Name the blood parasite species.
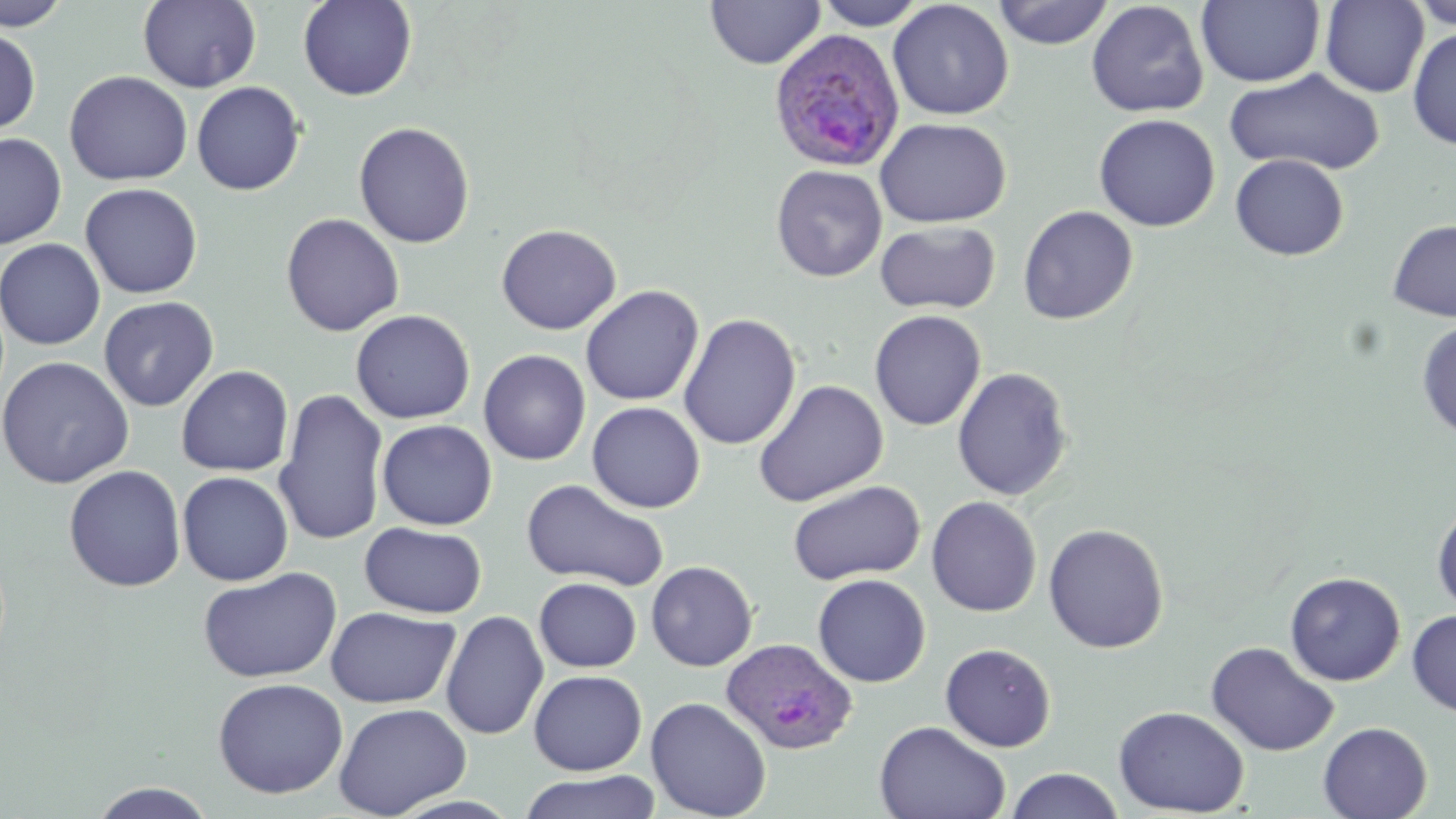

Plasmodium ovale.

uninfected red blood cell locations = approximate bounding boxes as (x1, y1, x2, y2) in pixels: (0, 0, 73, 31), (138, 0, 262, 93), (298, 0, 417, 101), (705, 0, 825, 69), (813, 0, 929, 30), (992, 0, 1114, 49), (1408, 0, 1455, 31), (888, 1, 1013, 120), (1086, 1, 1209, 118), (1196, 1, 1325, 87), (1320, 1, 1429, 97), (1407, 25, 1456, 150), (0, 26, 41, 137), (1224, 68, 1385, 177), (64, 71, 192, 186), (191, 81, 306, 196), (1093, 113, 1220, 232), (875, 117, 1011, 228), (353, 122, 475, 249), (0, 132, 67, 249), (1230, 154, 1348, 260), (771, 165, 887, 283), (80, 182, 203, 299), (1017, 205, 1138, 325), (280, 213, 404, 337), (1387, 218, 1456, 322), (875, 220, 1000, 315), (496, 224, 621, 335), (0, 238, 105, 350), (580, 285, 704, 406), (98, 296, 219, 412), (350, 309, 475, 424), (869, 309, 986, 431), (678, 313, 801, 450), (1416, 319, 1456, 439), (478, 349, 591, 466), (0, 356, 135, 489), (176, 365, 294, 477), (952, 367, 1073, 501), (753, 379, 888, 507), (273, 389, 390, 547), (586, 402, 705, 513), (376, 419, 497, 531), (63, 465, 186, 592), (177, 471, 294, 586), (521, 479, 670, 592), (787, 480, 925, 585), (926, 496, 1042, 617), (1432, 500, 1456, 615), (360, 522, 487, 618), (1043, 523, 1169, 653), (646, 561, 758, 671), (197, 567, 343, 684), (1285, 571, 1406, 685), (812, 574, 931, 687), (534, 577, 642, 672), (325, 606, 460, 708), (440, 610, 549, 741), (1407, 610, 1456, 718), (1205, 641, 1339, 756), (940, 643, 1056, 752), (528, 669, 647, 776), (212, 677, 348, 799), (645, 696, 771, 819), (333, 703, 472, 818), (1113, 705, 1249, 817), (874, 720, 1011, 819), (1318, 721, 1432, 819), (1004, 768, 1125, 819), (519, 770, 660, 819), (88, 781, 219, 818)
image size = 1456×819 pixels
stain = May-Grünwald-Giemsa
preparation = thin blood smear
Plasmodium ovale-infected red blood cell locations = approximate bounding boxes as (x1, y1, x2, y2) in pixels: (768, 29, 906, 172), (719, 636, 858, 754)
magnification = 1000x
field of view = single
modality = light microscopy